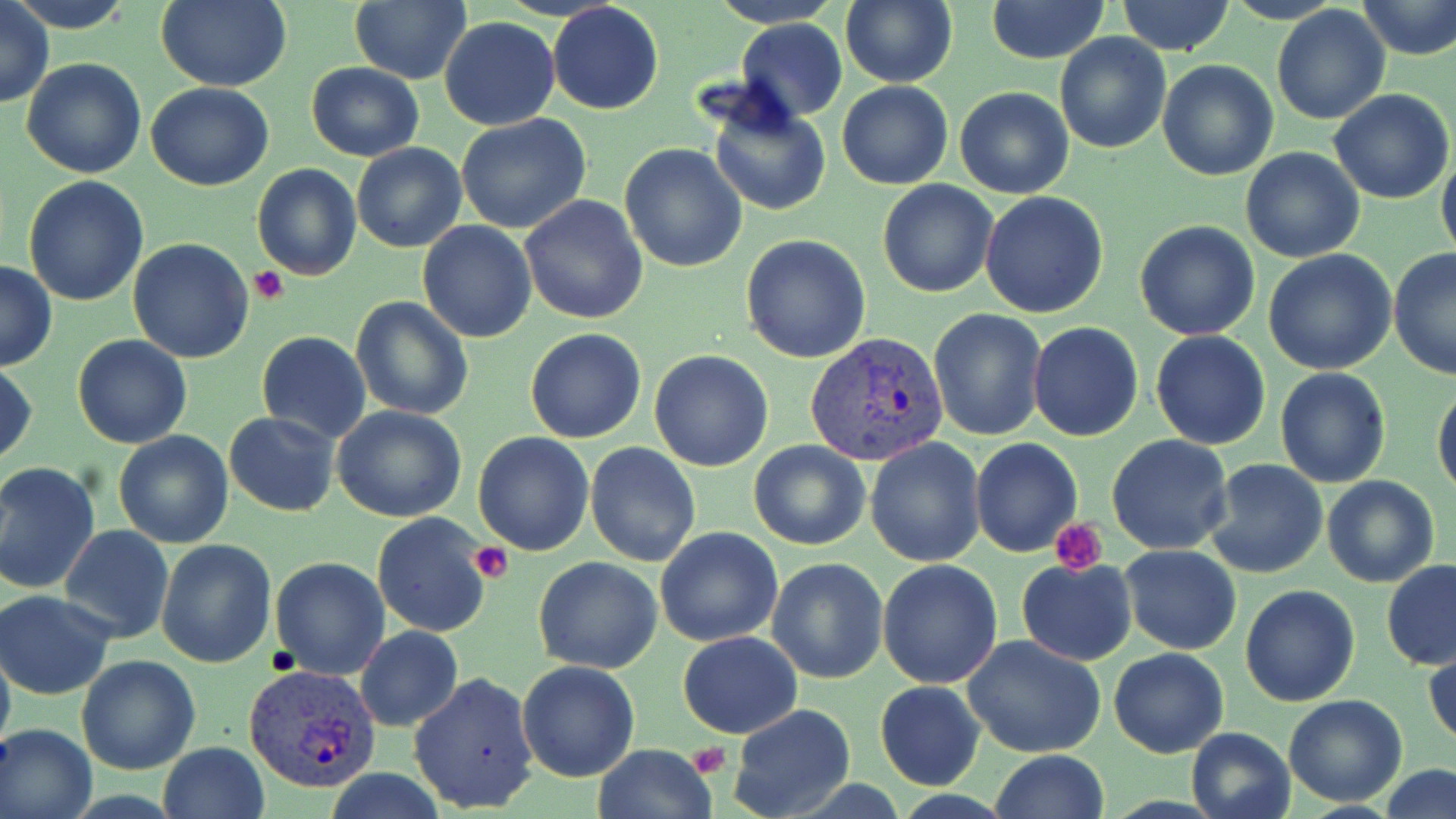

Approximate bounding boxes as [x1, y1, x2, y2] in pixels. Plasmodium vivax-infected red blood cell locations: [805, 330, 952, 466], [244, 664, 381, 793]. Uninfected red blood cell locations: [11, 0, 138, 31], [155, 0, 292, 91], [707, 0, 846, 28], [840, 0, 957, 88], [985, 0, 1111, 66], [1114, 0, 1236, 57], [0, 1, 53, 107], [349, 1, 472, 84], [1357, 1, 1456, 60], [548, 3, 664, 114], [1271, 4, 1391, 126], [439, 15, 559, 131], [737, 19, 846, 120], [1054, 32, 1173, 153], [21, 58, 147, 180], [1157, 59, 1278, 181], [306, 62, 425, 162], [837, 81, 953, 191], [145, 82, 274, 191], [955, 86, 1074, 198], [1329, 88, 1454, 205], [706, 93, 832, 219], [457, 115, 591, 235], [351, 142, 467, 253], [620, 143, 748, 272], [1240, 147, 1366, 263], [1436, 153, 1456, 266], [251, 164, 361, 281], [22, 175, 150, 307], [878, 179, 997, 297], [387, 180, 508, 331], [981, 193, 1111, 319], [518, 195, 649, 325], [1134, 219, 1261, 340], [417, 220, 538, 343], [740, 234, 871, 363], [127, 238, 255, 363], [1389, 247, 1456, 381], [1264, 249, 1397, 374], [0, 261, 57, 370], [351, 297, 475, 421], [928, 309, 1048, 442], [1028, 322, 1144, 441], [525, 329, 646, 444], [256, 330, 370, 443], [1150, 330, 1271, 449], [73, 335, 193, 450], [649, 349, 774, 471], [0, 360, 38, 468], [1274, 367, 1391, 489], [1433, 383, 1456, 499], [330, 404, 467, 523], [224, 411, 341, 517], [114, 431, 235, 548], [472, 432, 595, 555], [1106, 435, 1235, 556], [864, 437, 987, 566], [970, 438, 1082, 555], [748, 440, 871, 550], [585, 443, 702, 567], [1205, 459, 1329, 580], [0, 461, 101, 596], [1321, 476, 1439, 588], [372, 512, 493, 639], [60, 524, 174, 643], [655, 527, 783, 647], [155, 538, 276, 668], [1120, 544, 1242, 654], [270, 556, 391, 679], [533, 557, 663, 674], [767, 557, 887, 683], [1016, 557, 1137, 667], [877, 558, 1004, 689], [1382, 558, 1456, 670], [1240, 584, 1361, 706], [1, 591, 115, 698], [354, 626, 462, 730], [677, 632, 802, 738], [962, 634, 1106, 758], [0, 640, 15, 759], [1109, 646, 1229, 759], [1426, 648, 1456, 747], [76, 655, 201, 773], [516, 661, 640, 781], [409, 672, 541, 814], [874, 682, 985, 791], [1282, 694, 1407, 807], [729, 704, 857, 819], [1, 724, 97, 819], [1185, 726, 1297, 819], [159, 742, 269, 819], [591, 744, 718, 819], [990, 751, 1109, 819], [1378, 764, 1456, 819], [323, 771, 448, 818]. Platelet locations: [249, 266, 290, 305], [1052, 519, 1110, 573], [470, 544, 513, 584], [689, 744, 730, 775]. Slide-level diagnosis: Plasmodium vivax. Image is 1456×819 pixels. Thin blood smear. Captured at 1000x magnification. Single field of view. May-Grünwald-Giemsa stain. Light microscopy.